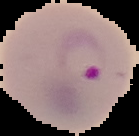
Result: Plasmodium parasites identified. From a thin blood smear. Cell region segmented out of the field of view; the surrounding area is masked to black. Image is 139×136 pixels.